Assess the morphology of the red blood cells.
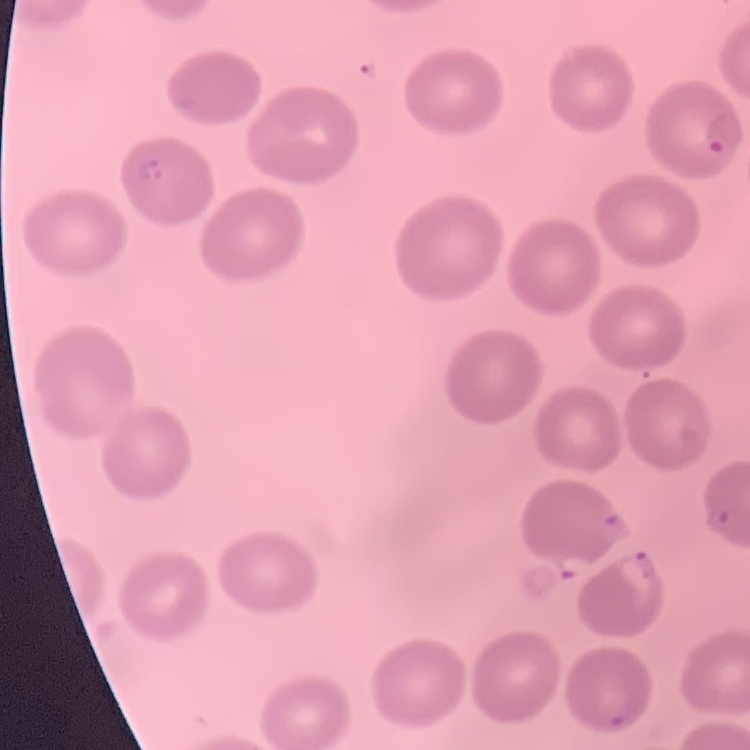

No rouleaux formation.

One tile cut from a larger photomicrograph. Stained with either Field's or Giemsa. Thin peripheral smear.